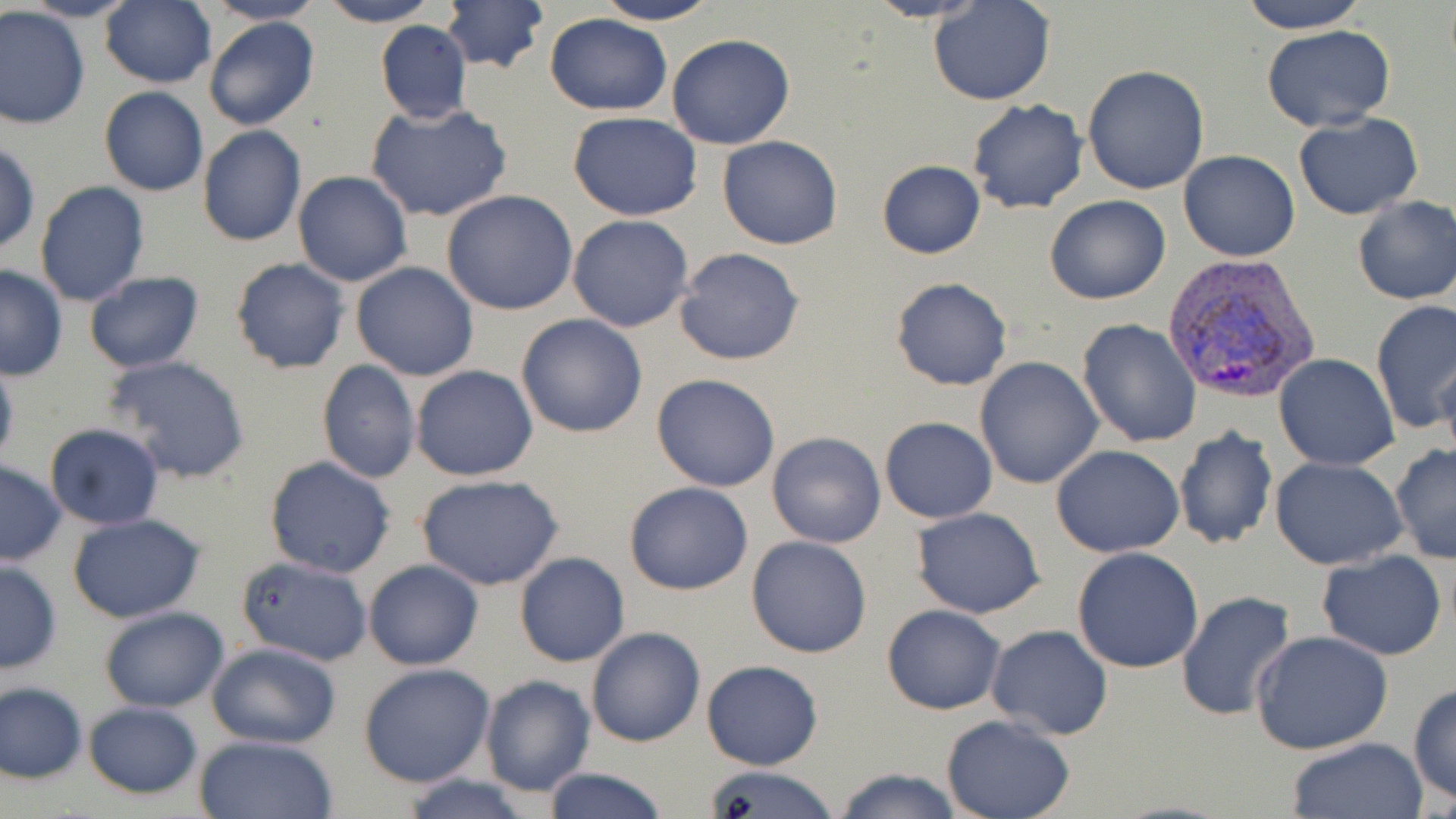 Approximate bounding boxes as (x1, y1, x2, y2) in pixels. Plasmodium vivax-infected red blood cell locations: (1165, 254, 1320, 404). Uninfected red blood cell locations: (21, 0, 141, 23), (99, 0, 215, 88), (204, 0, 326, 26), (316, 0, 439, 27), (593, 0, 722, 25), (863, 0, 989, 22), (929, 0, 1056, 106), (440, 1, 550, 75), (1238, 1, 1369, 33), (1, 7, 90, 131), (543, 13, 672, 115), (203, 16, 320, 131), (374, 19, 473, 123), (1261, 25, 1396, 132), (666, 34, 796, 150), (1082, 64, 1210, 194), (99, 87, 208, 196), (966, 99, 1089, 214), (366, 102, 515, 223), (569, 112, 702, 221), (1294, 113, 1422, 219), (197, 125, 306, 247), (718, 135, 843, 249), (1, 143, 40, 254), (1178, 148, 1300, 262), (876, 160, 986, 259), (293, 171, 413, 288), (34, 181, 150, 308), (441, 191, 581, 316), (1045, 195, 1170, 305), (1351, 195, 1456, 305), (567, 214, 694, 332), (674, 247, 806, 366), (229, 256, 351, 375), (350, 262, 480, 382), (0, 265, 68, 380), (82, 271, 205, 373), (890, 276, 1013, 392), (1371, 300, 1456, 436), (516, 313, 649, 439), (1077, 318, 1202, 447), (1431, 350, 1455, 458), (104, 354, 253, 484), (1274, 354, 1399, 472), (975, 356, 1105, 488), (0, 358, 19, 472), (316, 359, 420, 484), (410, 365, 539, 481), (650, 373, 781, 492), (880, 417, 998, 523), (43, 423, 165, 530), (1174, 426, 1278, 550), (766, 430, 887, 548), (1050, 445, 1185, 558), (1390, 445, 1456, 564), (263, 454, 397, 579), (1270, 457, 1407, 570), (0, 460, 67, 565), (415, 473, 566, 591), (623, 481, 753, 596), (911, 507, 1045, 617), (66, 511, 205, 623), (746, 535, 873, 659), (1072, 547, 1204, 673), (1315, 551, 1448, 660), (514, 552, 630, 667), (237, 557, 374, 666), (363, 559, 484, 671), (0, 560, 62, 674), (1175, 590, 1295, 723), (881, 604, 1006, 715), (99, 606, 229, 712), (984, 624, 1114, 742), (587, 627, 707, 747), (1251, 631, 1393, 755), (206, 641, 342, 748), (699, 660, 825, 770), (358, 663, 496, 786), (478, 674, 595, 797), (1, 682, 88, 783), (1409, 683, 1456, 805), (81, 701, 204, 799), (940, 715, 1077, 819), (192, 734, 338, 818), (1285, 737, 1426, 819), (698, 763, 841, 819), (540, 767, 668, 819), (829, 767, 964, 819), (393, 775, 540, 819). Slide-level diagnosis: Plasmodium vivax. Image is 1456×819 pixels. Thin blood film. May-Grünwald-Giemsa stain. Light microscopy. Single field of view. 1000x magnification.